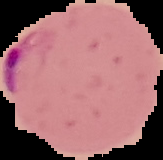

Summary:
  - Malaria status: parasitized
  - Preparation: thin blood film
  - Image type: segmented cell region on a black background
  - Image size: 163×160 pixels